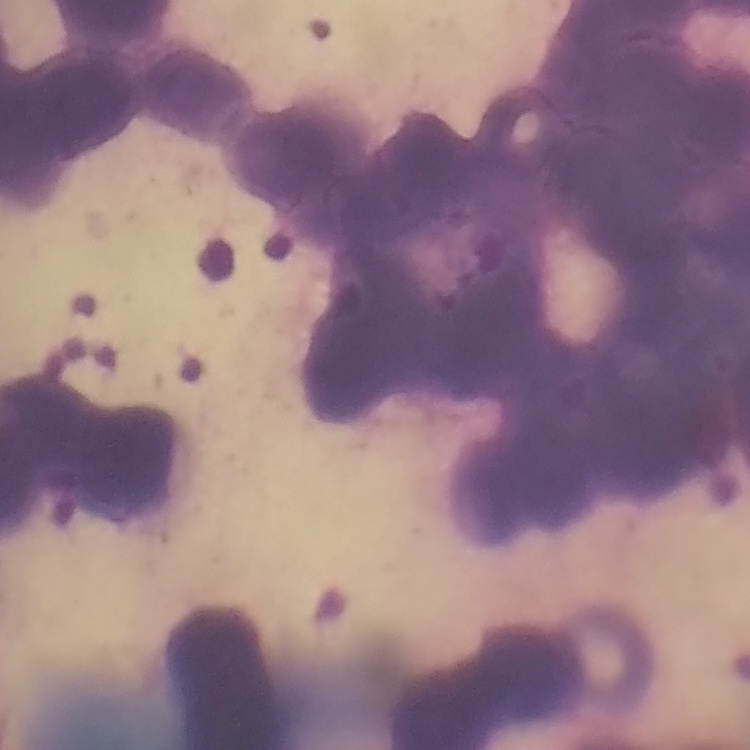

Summary:
  - Red blood cell morphology: rouleaux formation
  - Image type: one tile cut from a larger photomicrograph
  - Preparation: thin blood film
  - Stain: Field's or Giemsa